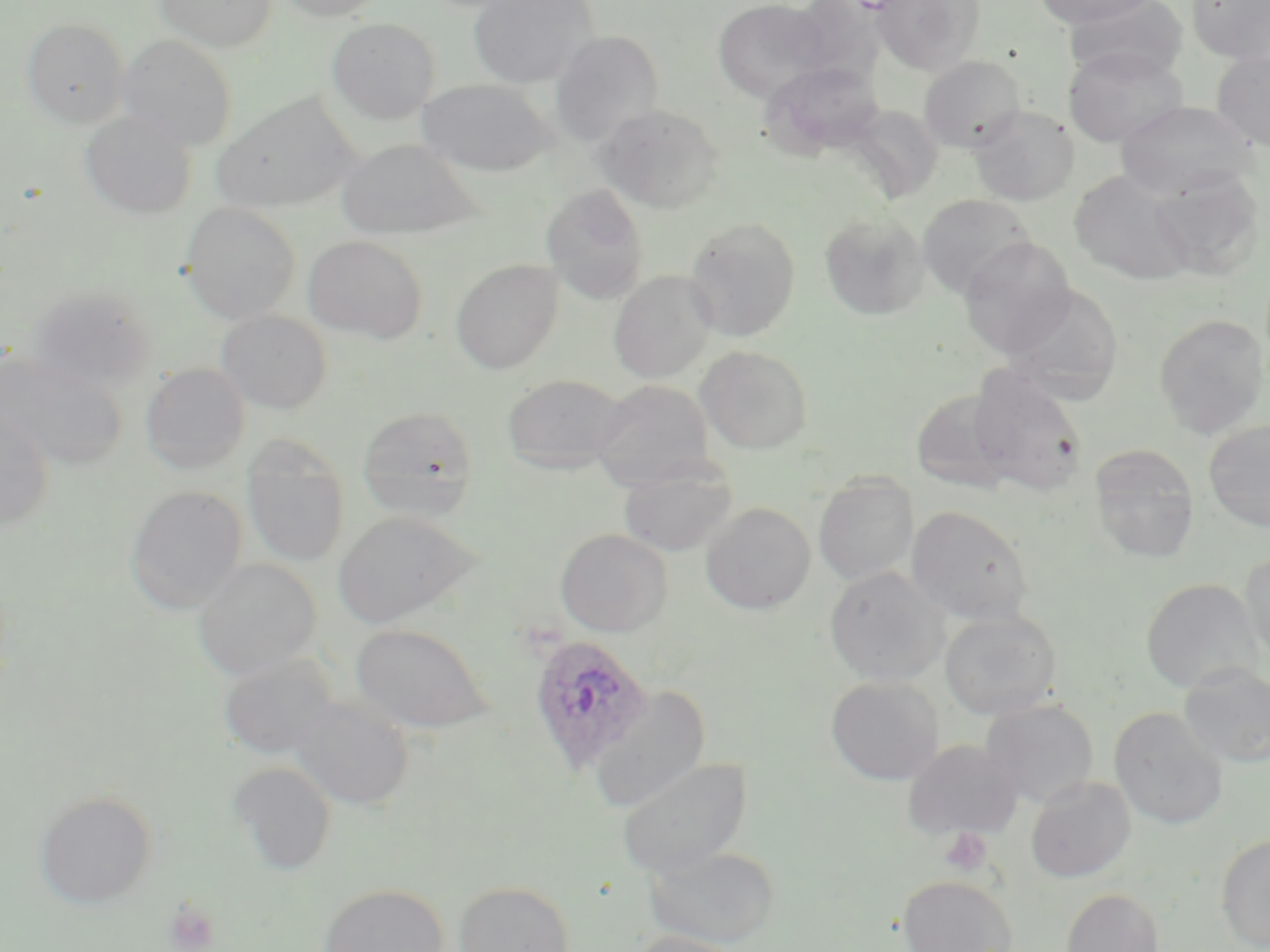
Approximate bounding boxes as named x1/y1/x2/y2 corners in pixels. Uninfected red blood cell locations: (x1=156, y1=0, x2=276, y2=52), (x1=277, y1=0, x2=387, y2=20), (x1=468, y1=0, x2=597, y2=88), (x1=712, y1=0, x2=830, y2=100), (x1=872, y1=0, x2=985, y2=75), (x1=1032, y1=0, x2=1158, y2=29), (x1=1064, y1=0, x2=1189, y2=82), (x1=1187, y1=0, x2=1270, y2=65), (x1=327, y1=17, x2=440, y2=125), (x1=22, y1=18, x2=129, y2=126), (x1=549, y1=31, x2=664, y2=146), (x1=117, y1=33, x2=238, y2=150), (x1=1063, y1=47, x2=1188, y2=148), (x1=1211, y1=50, x2=1270, y2=151), (x1=919, y1=55, x2=1026, y2=152), (x1=761, y1=61, x2=887, y2=159), (x1=416, y1=78, x2=553, y2=177), (x1=213, y1=92, x2=358, y2=213), (x1=1114, y1=99, x2=1260, y2=198), (x1=596, y1=103, x2=724, y2=213), (x1=969, y1=105, x2=1079, y2=206), (x1=80, y1=111, x2=197, y2=220), (x1=336, y1=138, x2=479, y2=240), (x1=1068, y1=169, x2=1200, y2=285), (x1=1147, y1=169, x2=1265, y2=280), (x1=541, y1=184, x2=650, y2=305), (x1=918, y1=194, x2=1036, y2=299), (x1=180, y1=202, x2=300, y2=323), (x1=819, y1=211, x2=930, y2=321), (x1=684, y1=217, x2=801, y2=341), (x1=303, y1=235, x2=428, y2=344), (x1=958, y1=237, x2=1077, y2=357), (x1=451, y1=258, x2=563, y2=373), (x1=608, y1=270, x2=716, y2=383), (x1=26, y1=283, x2=158, y2=394), (x1=1000, y1=283, x2=1124, y2=401), (x1=217, y1=310, x2=332, y2=413), (x1=1154, y1=314, x2=1268, y2=437), (x1=696, y1=345, x2=813, y2=454), (x1=0, y1=354, x2=127, y2=470), (x1=142, y1=363, x2=251, y2=474), (x1=968, y1=368, x2=1089, y2=497), (x1=502, y1=373, x2=631, y2=473), (x1=590, y1=379, x2=715, y2=489), (x1=910, y1=388, x2=1019, y2=494), (x1=358, y1=407, x2=479, y2=520), (x1=0, y1=412, x2=54, y2=529), (x1=1203, y1=419, x2=1270, y2=531), (x1=242, y1=442, x2=350, y2=568), (x1=1090, y1=446, x2=1199, y2=565), (x1=617, y1=461, x2=737, y2=558), (x1=813, y1=473, x2=919, y2=587), (x1=126, y1=484, x2=247, y2=613), (x1=700, y1=502, x2=816, y2=614), (x1=906, y1=505, x2=1034, y2=626), (x1=332, y1=510, x2=481, y2=629), (x1=555, y1=528, x2=673, y2=636), (x1=1239, y1=549, x2=1270, y2=671), (x1=193, y1=558, x2=322, y2=679), (x1=824, y1=566, x2=949, y2=686), (x1=1140, y1=577, x2=1264, y2=694), (x1=940, y1=610, x2=1062, y2=720), (x1=349, y1=622, x2=495, y2=735), (x1=218, y1=654, x2=339, y2=760), (x1=1179, y1=664, x2=1270, y2=768), (x1=826, y1=676, x2=944, y2=786), (x1=588, y1=685, x2=711, y2=812), (x1=291, y1=696, x2=414, y2=810), (x1=980, y1=698, x2=1099, y2=809), (x1=1109, y1=707, x2=1228, y2=829), (x1=902, y1=739, x2=1023, y2=841), (x1=617, y1=756, x2=753, y2=879), (x1=229, y1=761, x2=337, y2=875), (x1=1025, y1=776, x2=1136, y2=883), (x1=34, y1=790, x2=157, y2=909), (x1=1215, y1=833, x2=1270, y2=951), (x1=644, y1=845, x2=780, y2=948), (x1=897, y1=875, x2=1017, y2=952), (x1=454, y1=880, x2=576, y2=952), (x1=318, y1=883, x2=450, y2=952), (x1=1061, y1=887, x2=1165, y2=952), (x1=622, y1=931, x2=754, y2=952). Plasmodium ovale-infected red blood cell locations: (x1=526, y1=633, x2=655, y2=773). Platelet locations: (x1=939, y1=827, x2=994, y2=876), (x1=165, y1=898, x2=220, y2=952). Slide-level diagnosis: Plasmodium ovale. Image is 1270×952 pixels. May-Grünwald-Giemsa stain. Captured at 1000x magnification. Thin blood film. Single field of view. Light microscopy.